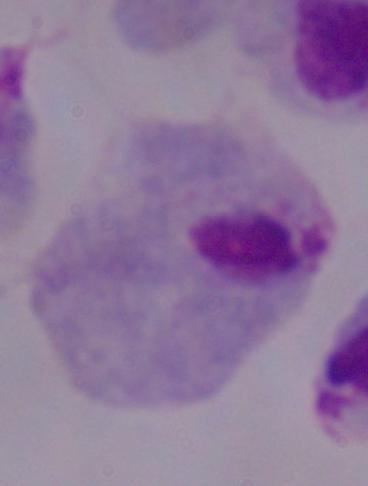

magnification = 1000x
modality = micrograph
identification = trichomonad